Mark where platelets are.
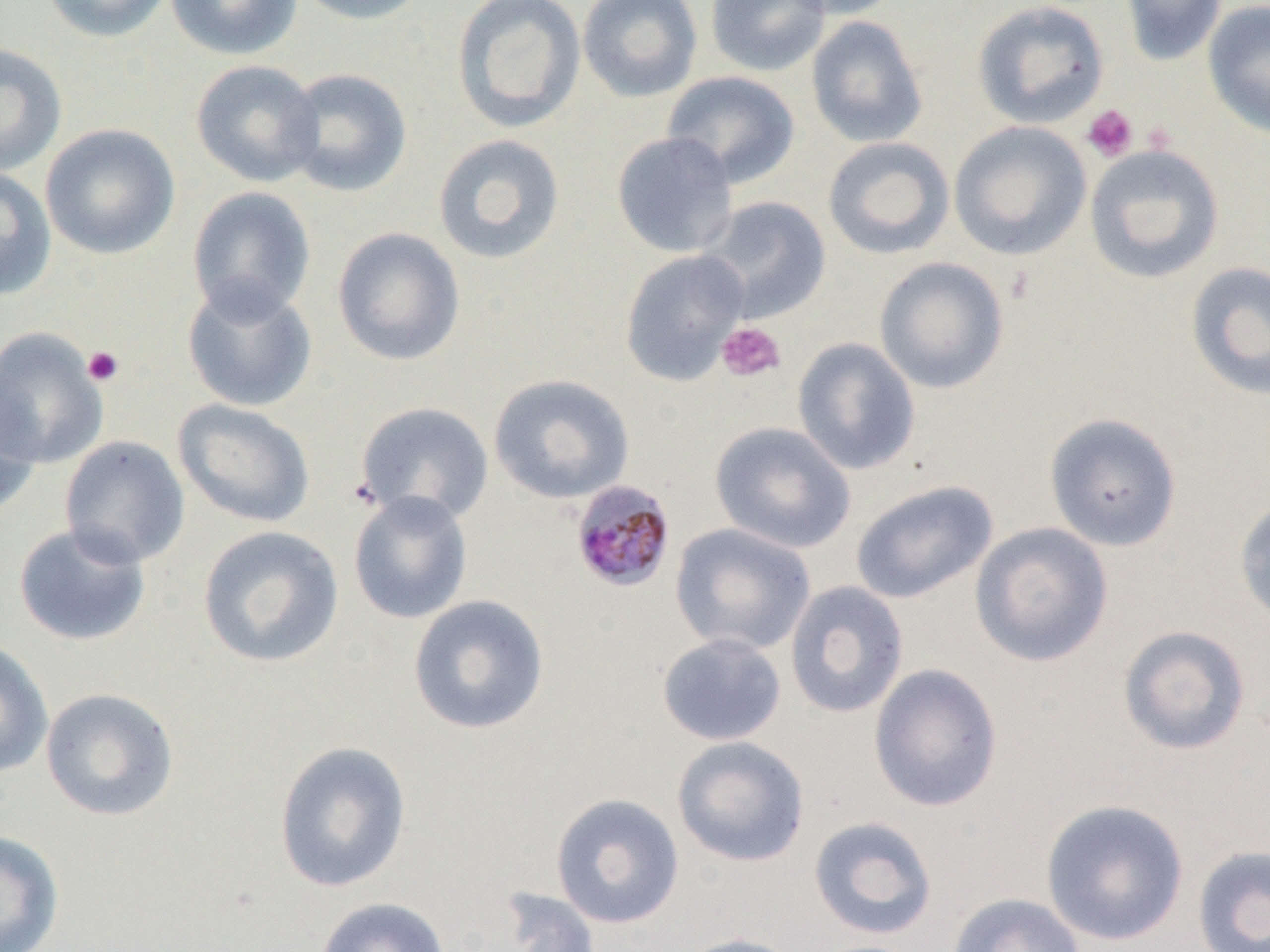
Approximate bounding boxes as (x1, y1, x2, y2) in pixels.
Platelets: (1082, 105, 1139, 162), (716, 322, 786, 383), (82, 346, 124, 386).

Plasmodium malariae-infected red blood cell locations: (571, 480, 676, 592). Uninfected red blood cell locations: (40, 0, 173, 43), (165, 0, 303, 61), (290, 0, 431, 25), (450, 0, 587, 134), (577, 0, 702, 102), (705, 0, 830, 77), (778, 0, 902, 20), (971, 0, 1110, 130), (1120, 0, 1227, 66), (1202, 0, 1270, 139), (806, 16, 928, 148), (0, 43, 67, 175), (190, 60, 324, 188), (281, 67, 412, 197), (662, 71, 800, 189), (949, 120, 1092, 261), (41, 124, 180, 259), (611, 131, 739, 259), (432, 134, 566, 265), (823, 136, 955, 260), (1084, 143, 1225, 284), (0, 166, 57, 300), (186, 186, 317, 323), (699, 196, 832, 323), (331, 227, 466, 367), (619, 250, 749, 387), (874, 257, 1009, 394), (1185, 260, 1270, 401), (181, 279, 317, 413), (0, 328, 108, 469), (792, 337, 921, 475), (0, 369, 42, 521), (488, 373, 635, 504), (173, 399, 315, 528), (355, 401, 494, 526), (1044, 412, 1182, 552), (710, 421, 855, 554), (59, 435, 190, 568), (850, 479, 998, 605), (348, 490, 473, 625), (1234, 494, 1270, 628), (13, 521, 152, 647), (670, 522, 816, 656), (970, 522, 1114, 667), (197, 525, 344, 669), (784, 581, 909, 719), (407, 593, 550, 735), (1117, 625, 1252, 756), (656, 632, 787, 746), (0, 639, 54, 777), (868, 663, 1003, 812), (40, 687, 180, 822), (672, 735, 810, 867), (273, 740, 412, 892), (550, 793, 684, 929), (1040, 799, 1190, 946), (808, 815, 938, 940), (0, 830, 64, 951), (1192, 845, 1270, 952), (495, 886, 602, 952), (946, 892, 1086, 952), (314, 896, 451, 952), (672, 933, 808, 952). Slide-level diagnosis: Plasmodium malariae. 1000x magnification. One field of a larger specimen. Thin blood smear. Image is 1270×952 pixels. Light microscopy.